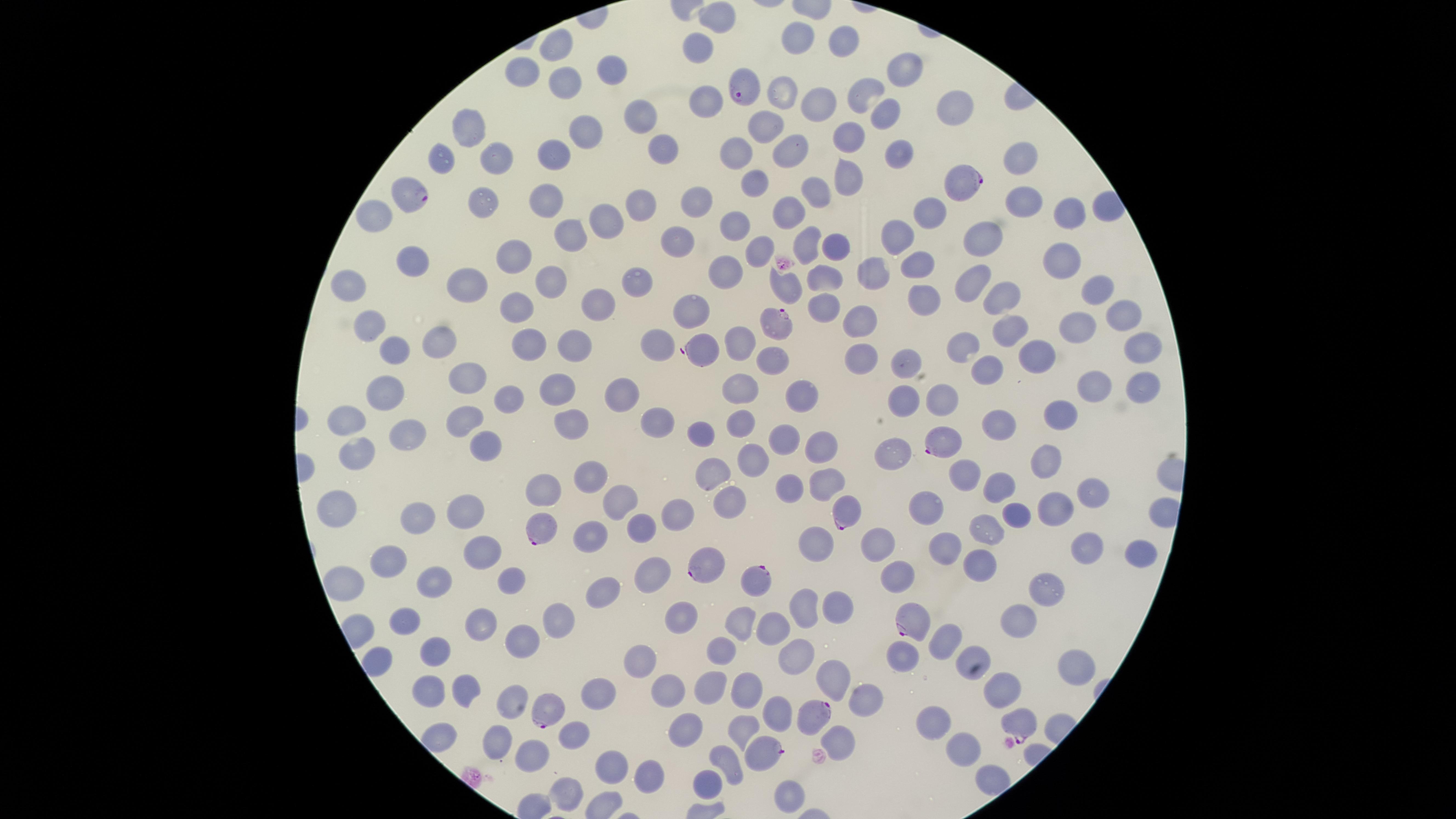
Approximate marker points as [x, y] in pixels. Parasitized red blood cells: [744, 89], [967, 187], [413, 200], [774, 318], [703, 351], [939, 441], [841, 510], [542, 531], [701, 567], [755, 581], [907, 624], [549, 709], [811, 720], [1022, 727], [764, 753]. Uninfected red blood cells: [713, 21], [798, 37], [841, 39], [558, 41], [696, 50], [908, 69], [612, 70], [524, 71], [567, 81], [782, 91], [866, 93], [817, 100], [702, 101], [955, 103], [638, 116], [884, 118], [768, 128], [586, 129], [474, 130], [848, 137], [666, 142], [790, 150], [898, 151], [736, 152], [557, 153], [494, 156], [442, 158], [1015, 159], [755, 180], [846, 180], [812, 190], [693, 197], [548, 198], [644, 199], [485, 200], [1020, 203], [929, 206], [1065, 208], [787, 209], [375, 213], [615, 218], [735, 225], [568, 233], [980, 236], [897, 238], [677, 240], [805, 240], [833, 245], [752, 248], [416, 258], [514, 259], [914, 261], [1065, 261], [874, 268], [825, 275], [966, 275], [728, 276], [547, 277], [639, 279], [471, 281], [351, 287], [789, 289], [1095, 290], [1007, 292], [927, 295], [520, 302], [596, 306], [823, 306], [689, 308], [1121, 317], [1075, 320], [858, 322], [1007, 329], [367, 333], [439, 337], [741, 339], [576, 345], [660, 345], [968, 345], [528, 346], [1138, 348], [392, 351], [775, 357], [1041, 358], [858, 361], [898, 366], [987, 371], [470, 378], [746, 385], [1095, 385], [1139, 387], [386, 391], [555, 392], [800, 396], [905, 398], [508, 399], [942, 401], [626, 402], [1061, 413], [347, 414], [570, 416], [742, 420], [462, 421], [997, 421], [658, 428], [693, 431], [401, 435], [784, 438], [483, 445], [819, 447], [895, 451], [751, 460], [1046, 462], [719, 473], [587, 474], [965, 476], [823, 483], [1003, 485], [793, 486], [547, 489], [1091, 494], [622, 498], [338, 499], [725, 503], [926, 508], [1052, 508], [464, 512], [416, 515], [679, 515], [1015, 519], [642, 522], [986, 533], [589, 534], [877, 543], [943, 544], [816, 545], [1082, 548], [1134, 552], [391, 553], [477, 555], [978, 558], [644, 572], [900, 572], [514, 580], [342, 581], [438, 582], [602, 588], [1046, 588], [841, 606], [807, 607], [1018, 617], [684, 618], [557, 620], [480, 622], [738, 623], [412, 625], [781, 629], [523, 639], [942, 641], [434, 649], [723, 649], [904, 653], [645, 656], [793, 657], [374, 660], [1067, 667], [835, 675], [668, 686], [711, 686], [1000, 686], [748, 687], [598, 688], [430, 691], [465, 691], [512, 698], [859, 701], [777, 713], [933, 723], [741, 727], [570, 733], [689, 733], [435, 734], [842, 735], [494, 740], [964, 748], [528, 750], [612, 759], [729, 761], [999, 773], [646, 776], [707, 781], [563, 789], [785, 796]. One field of view of the specimen. The visible region is circular. Presence: malaria parasites detected. Giemsa stain. Species: Plasmodium falciparum. Photographed with a smartphone camera through the microscope eyepiece. Thin smear of blood. Image is 1456×819 pixels.